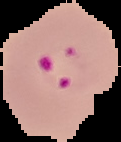
Result: Plasmodium parasites identified. Segmented cell region on a black background. From a thin blood film. Image is 121×142 pixels.